Outline each Trypanosoma brucei.
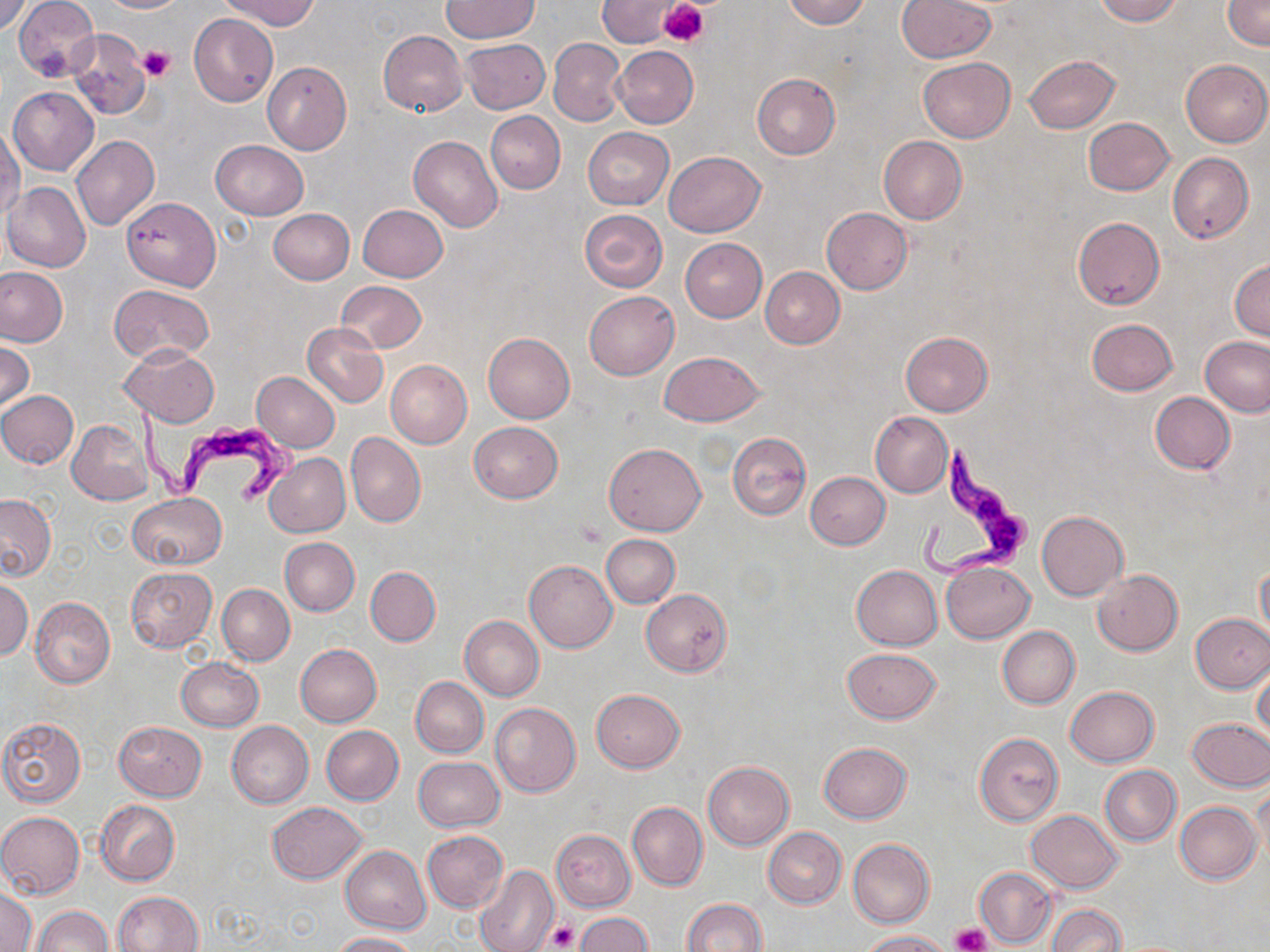
Approximate bounding boxes as named x1/y1/x2/y2 corners in pixels.
Trypanosoma brucei: (x1=131, y1=401, x2=299, y2=506), (x1=909, y1=442, x2=1036, y2=591).

Summary:
  - Uninfected red blood cell locations: (x1=0, y1=0, x2=29, y2=36), (x1=100, y1=0, x2=186, y2=13), (x1=222, y1=0, x2=319, y2=31), (x1=599, y1=0, x2=677, y2=47), (x1=784, y1=0, x2=870, y2=29), (x1=897, y1=0, x2=995, y2=62), (x1=1093, y1=0, x2=1181, y2=24), (x1=1223, y1=0, x2=1269, y2=49), (x1=14, y1=1, x2=98, y2=82), (x1=441, y1=1, x2=539, y2=43), (x1=189, y1=14, x2=277, y2=106), (x1=66, y1=28, x2=149, y2=119), (x1=378, y1=30, x2=467, y2=116), (x1=460, y1=38, x2=550, y2=115), (x1=549, y1=38, x2=624, y2=126), (x1=611, y1=46, x2=698, y2=128), (x1=1023, y1=55, x2=1119, y2=133), (x1=917, y1=57, x2=1015, y2=142), (x1=1180, y1=58, x2=1270, y2=147), (x1=262, y1=61, x2=351, y2=154), (x1=752, y1=74, x2=840, y2=159), (x1=8, y1=86, x2=99, y2=177), (x1=486, y1=111, x2=565, y2=193), (x1=1084, y1=117, x2=1176, y2=195), (x1=1, y1=123, x2=23, y2=218), (x1=583, y1=128, x2=673, y2=209), (x1=71, y1=135, x2=160, y2=231), (x1=409, y1=135, x2=502, y2=231), (x1=879, y1=137, x2=966, y2=224), (x1=210, y1=140, x2=308, y2=220), (x1=665, y1=151, x2=765, y2=237), (x1=1167, y1=152, x2=1253, y2=243), (x1=2, y1=181, x2=91, y2=272), (x1=121, y1=196, x2=221, y2=291), (x1=358, y1=203, x2=447, y2=283), (x1=821, y1=207, x2=912, y2=294), (x1=268, y1=209, x2=355, y2=284), (x1=578, y1=209, x2=667, y2=291), (x1=1072, y1=216, x2=1165, y2=310), (x1=680, y1=238, x2=768, y2=322), (x1=1230, y1=259, x2=1270, y2=340), (x1=0, y1=267, x2=69, y2=347), (x1=761, y1=267, x2=845, y2=348), (x1=336, y1=281, x2=423, y2=353), (x1=109, y1=283, x2=215, y2=366), (x1=584, y1=291, x2=678, y2=379), (x1=1086, y1=318, x2=1177, y2=396), (x1=303, y1=323, x2=388, y2=408), (x1=483, y1=332, x2=574, y2=422), (x1=901, y1=332, x2=992, y2=415), (x1=1199, y1=336, x2=1270, y2=418), (x1=0, y1=342, x2=33, y2=414), (x1=120, y1=345, x2=219, y2=425), (x1=277, y1=345, x2=386, y2=446), (x1=660, y1=351, x2=764, y2=426), (x1=385, y1=360, x2=473, y2=448), (x1=252, y1=372, x2=341, y2=451), (x1=0, y1=390, x2=79, y2=469), (x1=1150, y1=392, x2=1236, y2=473), (x1=869, y1=411, x2=952, y2=497), (x1=68, y1=420, x2=153, y2=504), (x1=469, y1=422, x2=563, y2=502), (x1=346, y1=432, x2=425, y2=527), (x1=727, y1=432, x2=810, y2=521), (x1=603, y1=442, x2=706, y2=535), (x1=264, y1=452, x2=350, y2=539), (x1=805, y1=471, x2=890, y2=549), (x1=128, y1=492, x2=226, y2=569), (x1=0, y1=494, x2=56, y2=581), (x1=1037, y1=510, x2=1128, y2=600), (x1=602, y1=534, x2=679, y2=607), (x1=280, y1=537, x2=360, y2=615), (x1=524, y1=559, x2=617, y2=652), (x1=1256, y1=560, x2=1270, y2=643), (x1=942, y1=562, x2=1034, y2=642), (x1=851, y1=565, x2=942, y2=650), (x1=125, y1=566, x2=216, y2=652), (x1=366, y1=566, x2=440, y2=647), (x1=1093, y1=569, x2=1183, y2=655), (x1=0, y1=579, x2=32, y2=661), (x1=217, y1=584, x2=295, y2=665), (x1=641, y1=590, x2=732, y2=675), (x1=30, y1=596, x2=116, y2=688), (x1=1190, y1=613, x2=1270, y2=692), (x1=460, y1=617, x2=544, y2=699), (x1=997, y1=626, x2=1080, y2=708), (x1=295, y1=643, x2=381, y2=727), (x1=843, y1=649, x2=942, y2=723), (x1=175, y1=658, x2=263, y2=731), (x1=1252, y1=666, x2=1270, y2=745), (x1=410, y1=677, x2=488, y2=758), (x1=1066, y1=686, x2=1159, y2=766), (x1=592, y1=688, x2=685, y2=771), (x1=490, y1=703, x2=581, y2=797), (x1=0, y1=717, x2=87, y2=807), (x1=1185, y1=718, x2=1270, y2=790), (x1=227, y1=720, x2=313, y2=808), (x1=114, y1=721, x2=206, y2=800), (x1=320, y1=725, x2=403, y2=805), (x1=974, y1=733, x2=1063, y2=826), (x1=819, y1=742, x2=912, y2=822), (x1=414, y1=755, x2=504, y2=831), (x1=704, y1=761, x2=794, y2=850), (x1=1099, y1=765, x2=1181, y2=847), (x1=1250, y1=785, x2=1269, y2=867), (x1=96, y1=801, x2=179, y2=886), (x1=1175, y1=801, x2=1260, y2=884), (x1=268, y1=802, x2=366, y2=884), (x1=628, y1=802, x2=707, y2=891), (x1=1026, y1=810, x2=1123, y2=893), (x1=0, y1=811, x2=84, y2=898), (x1=763, y1=827, x2=846, y2=909), (x1=550, y1=829, x2=634, y2=911), (x1=422, y1=830, x2=508, y2=912), (x1=848, y1=839, x2=935, y2=928), (x1=342, y1=845, x2=431, y2=935), (x1=474, y1=863, x2=559, y2=952), (x1=974, y1=867, x2=1055, y2=948), (x1=1, y1=889, x2=36, y2=951), (x1=113, y1=891, x2=202, y2=952), (x1=682, y1=899, x2=767, y2=952), (x1=1045, y1=904, x2=1127, y2=952), (x1=33, y1=906, x2=113, y2=952), (x1=575, y1=911, x2=653, y2=951), (x1=861, y1=930, x2=949, y2=951), (x1=331, y1=932, x2=416, y2=952)
  - Platelet locations: (x1=659, y1=0, x2=707, y2=45), (x1=137, y1=44, x2=176, y2=80), (x1=575, y1=522, x2=607, y2=548), (x1=546, y1=923, x2=577, y2=951), (x1=952, y1=924, x2=990, y2=952)
  - Slide-level diagnosis: Trypanosoma brucei
  - Field of view: single
  - Modality: light microscopy
  - Magnification: 1000x
  - Stain: May-Grünwald-Giemsa
  - Image size: 1270×952 pixels
  - Preparation: thin blood film